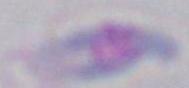
identification: Toxoplasma gondii
magnification: 1000x
modality: micrograph